State which parasite is depicted.
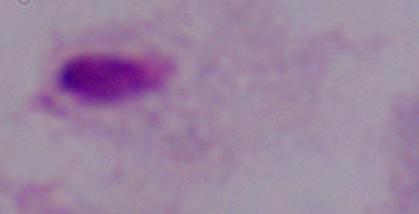

A trichomonad.

Summary:
  - Magnification: 1000x
  - Modality: micrograph